Identify the parasite.
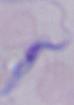

A trypanosome.

modality = micrograph
magnification = 1000x